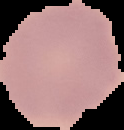
Image is 124×130 pixels. From a thin blood smear. Segmented cell region on a black background. Result: no malaria parasites seen.